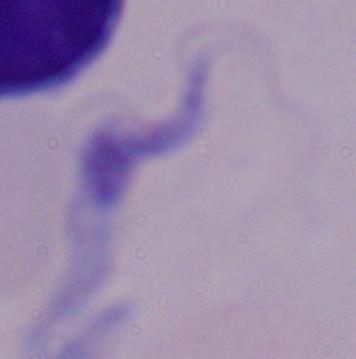

{
  "modality": "photomicrograph",
  "magnification": "1000x",
  "identification": "trypanosome"
}